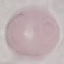
result = negative for malaria parasites
image type = cell patch, automatically extracted from a larger field of view and resized to 64 × 64 pixels
stain = Giemsa
preparation = thin blood smear
capture = smartphone camera at the microscope eyepiece